Assess the morphology of the red blood cells.
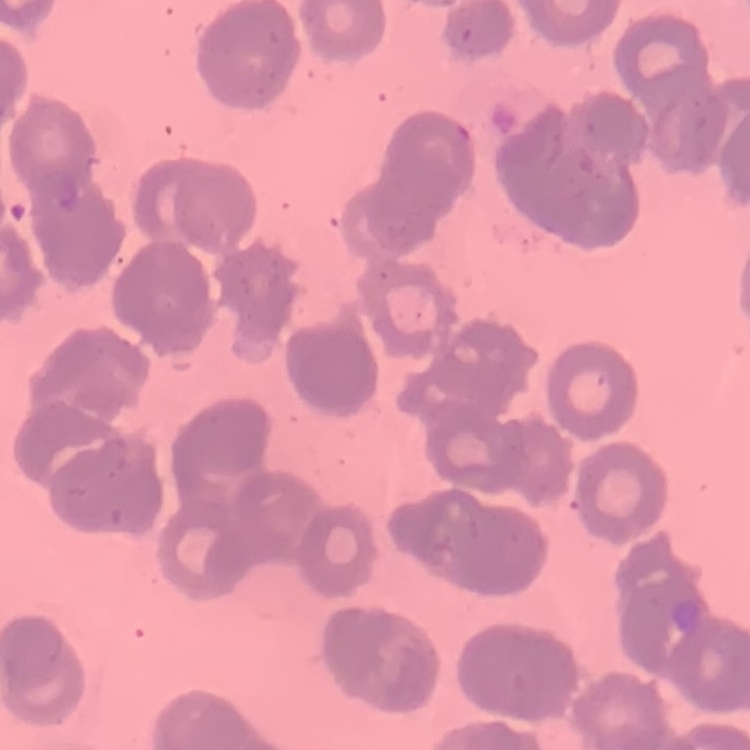

Rouleaux formation.

Summary:
  - Preparation: thin blood film
  - Image type: square crop of a larger photomicrograph
  - Stain: Field's or Giemsa